Assess this cell for malaria.
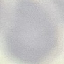
It is uninfected.

Summary:
  - Preparation: thin blood film
  - Stain: Giemsa
  - Capture: smartphone through the microscope eyepiece
  - Image type: cell patch, automatically extracted from a larger field of view and resized to 64 × 64 pixels